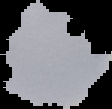
Image is 112×109 pixels. The area outside the segmented cell region is set to black. Malaria status: uninfected. From a thin blood film.